Comment on the morphology of the erythrocytes.
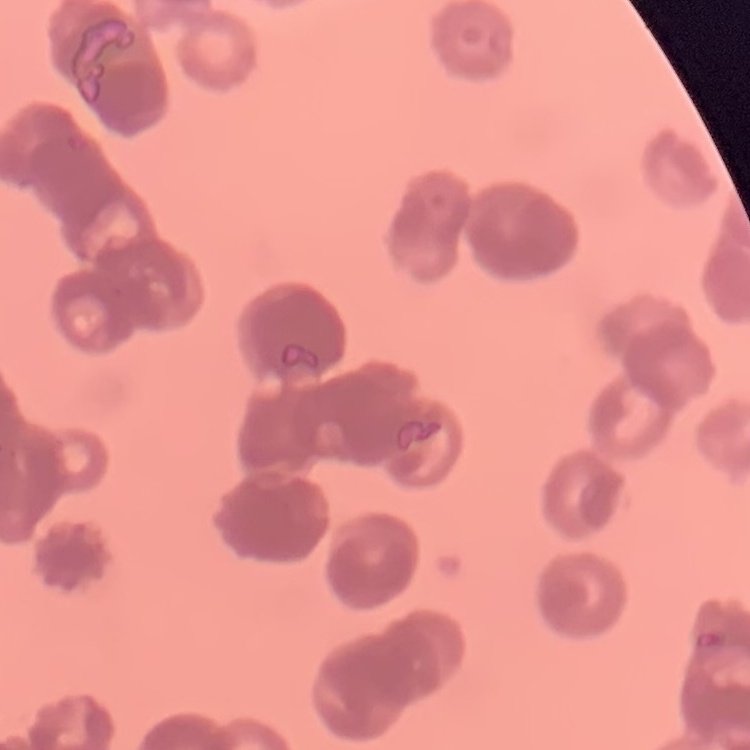
They show rouleaux formation.

{
  "preparation": "thin peripheral smear",
  "stain": "Field's or Giemsa",
  "image_type": "one tile cut from a larger photomicrograph"
}